State which cell type is depicted.
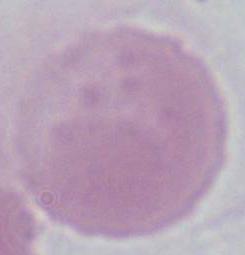

An erythrocyte.

modality: micrograph
magnification: 1000x